Locate every uninfected red blood cell.
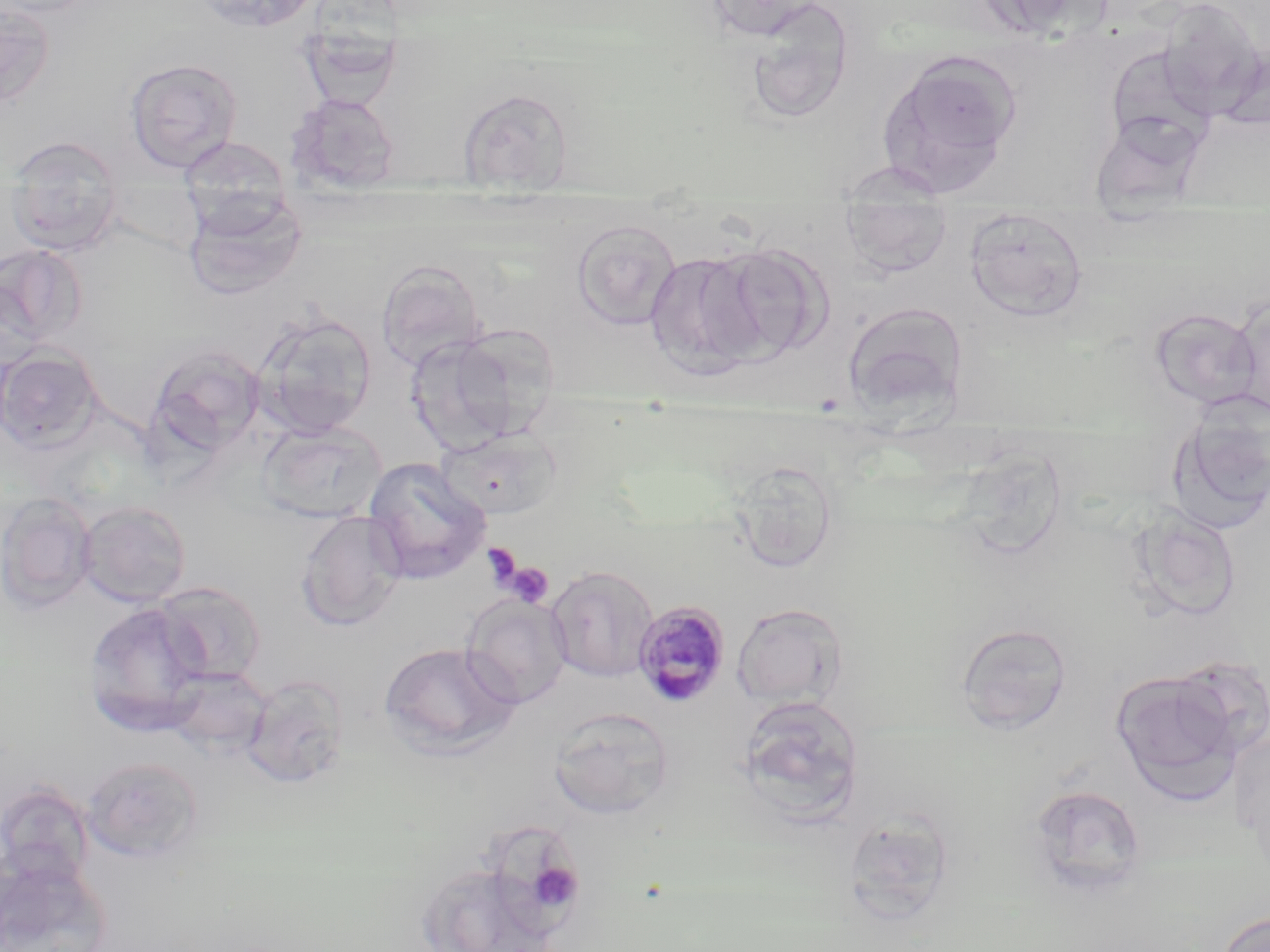

Approximate bounding boxes as (x1,y1)-(x2,y2) corner pairs in pixels.
Uninfected red blood cells: (187,0)-(324,34), (705,0)-(825,41), (973,0)-(1112,37), (0,1)-(56,110), (745,2)-(854,124), (297,27)-(404,112), (1104,45)-(1218,157), (877,50)-(1022,191), (125,57)-(244,173), (458,88)-(573,193), (285,93)-(401,194), (1086,113)-(1205,207), (3,136)-(125,257), (176,137)-(294,219), (832,161)-(954,204), (184,192)-(307,301), (840,205)-(953,279), (965,209)-(1088,324), (571,219)-(682,332), (710,243)-(831,360), (0,244)-(87,351), (644,251)-(768,378), (376,259)-(487,369), (1,277)-(45,373), (1229,294)-(1269,417), (840,301)-(970,419), (1148,307)-(1263,409), (251,309)-(377,437), (404,332)-(529,454), (147,344)-(266,457), (1,347)-(104,455), (1167,393)-(1270,533), (256,420)-(387,523), (436,428)-(562,521), (962,436)-(1070,562), (362,457)-(491,585), (729,461)-(840,573), (0,492)-(96,614), (77,501)-(192,607), (1127,508)-(1243,622), (295,510)-(408,632), (546,565)-(659,682), (153,581)-(266,686), (462,595)-(572,708), (83,601)-(212,736), (732,603)-(849,708), (955,622)-(1073,734), (378,641)-(519,755), (164,666)-(273,757), (1110,669)-(1243,802), (242,675)-(350,788), (736,695)-(865,822), (548,707)-(675,820), (82,756)-(204,863), (0,782)-(95,890), (1029,784)-(1148,898), (843,812)-(955,927), (484,815)-(593,932), (1,855)-(112,952), (426,864)-(554,949), (1215,910)-(1270,952).

Summary:
  - Plasmodium malariae-infected red blood cell locations: (632,600)-(731,708)
  - Platelet locations: (481,542)-(523,592), (504,561)-(555,608), (538,864)-(583,909)
  - Slide-level diagnosis: Plasmodium malariae
  - Stain: May-Grünwald-Giemsa
  - Image size: 1270×952 pixels
  - Magnification: 1000x
  - Field of view: one of a larger specimen
  - Modality: optical microscopy
  - Preparation: thin blood film